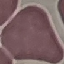 Result: no malaria parasites seen. Thin smear of blood. Giemsa-stained preparation. Photographed with a smartphone camera at the microscope eyepiece. Cell patch, automatically extracted from a larger field of view and resized to 64 × 64 pixels.